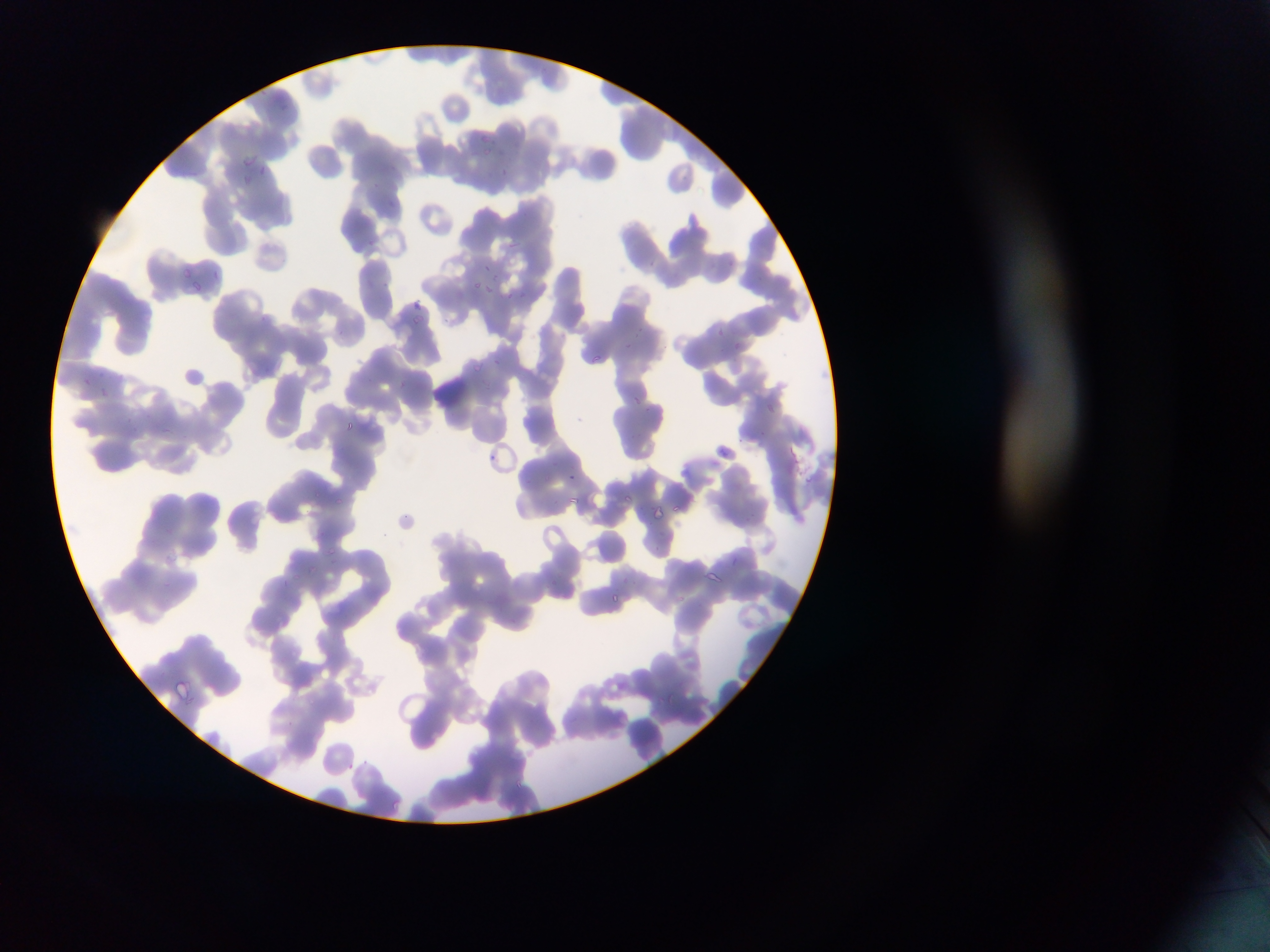
Approximate bounding boxes as [left, top, right, bottom] in pixels.
Summary:
  - Plasmodium parasite locations: [478, 130, 494, 146], [481, 146, 494, 156], [243, 152, 262, 168], [257, 165, 265, 176], [502, 165, 514, 182], [241, 173, 253, 183], [508, 242, 522, 250], [481, 261, 488, 269], [178, 265, 191, 277], [212, 270, 222, 284], [490, 271, 497, 283], [189, 279, 203, 296], [472, 279, 484, 295], [484, 282, 494, 296], [519, 290, 528, 298], [504, 292, 514, 302], [410, 297, 428, 308], [410, 313, 427, 323], [716, 327, 727, 335], [632, 330, 642, 340], [735, 336, 744, 350], [625, 342, 631, 350], [590, 353, 602, 364], [472, 361, 484, 371], [630, 393, 646, 408], [763, 397, 775, 414], [344, 420, 357, 432], [758, 430, 769, 436], [737, 437, 745, 444], [719, 447, 732, 462], [485, 451, 501, 468], [568, 471, 578, 483], [313, 487, 322, 499], [622, 490, 632, 505], [568, 492, 583, 507], [332, 497, 349, 512], [673, 502, 683, 514], [640, 503, 645, 513], [652, 504, 666, 524], [748, 511, 760, 520], [651, 542, 667, 557], [324, 546, 340, 556], [732, 555, 745, 565], [305, 565, 317, 573], [703, 571, 723, 586], [288, 573, 302, 584], [622, 576, 630, 582], [623, 577, 637, 585], [549, 578, 563, 584], [475, 583, 484, 596], [612, 593, 626, 603], [675, 595, 685, 603], [168, 677, 196, 704], [668, 691, 675, 710], [288, 720, 296, 727], [359, 757, 369, 765], [347, 763, 358, 772], [514, 779, 526, 790], [390, 797, 404, 815] | approximate [x, y] pixel centers of objects too small to bound: [407, 515]
  - Field of view: single
  - Preparation: thin blood film
  - Image size: 1270×952 pixels
  - Country: Ghana
  - Capture: mobile-phone photograph through a microscope